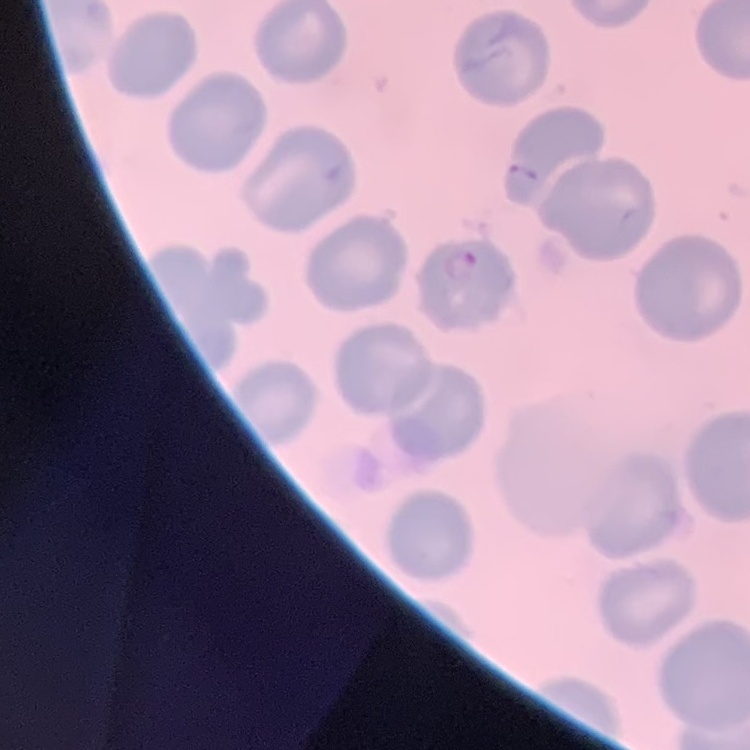
The red blood cells show no rouleaux formation. Square crop of a larger photomicrograph. Stained with either Field's or Giemsa. Thin blood smear.